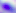

Micrograph. Toxoplasma gondii is seen. Captured at 400x magnification.